Locate and identify every blood parasite.
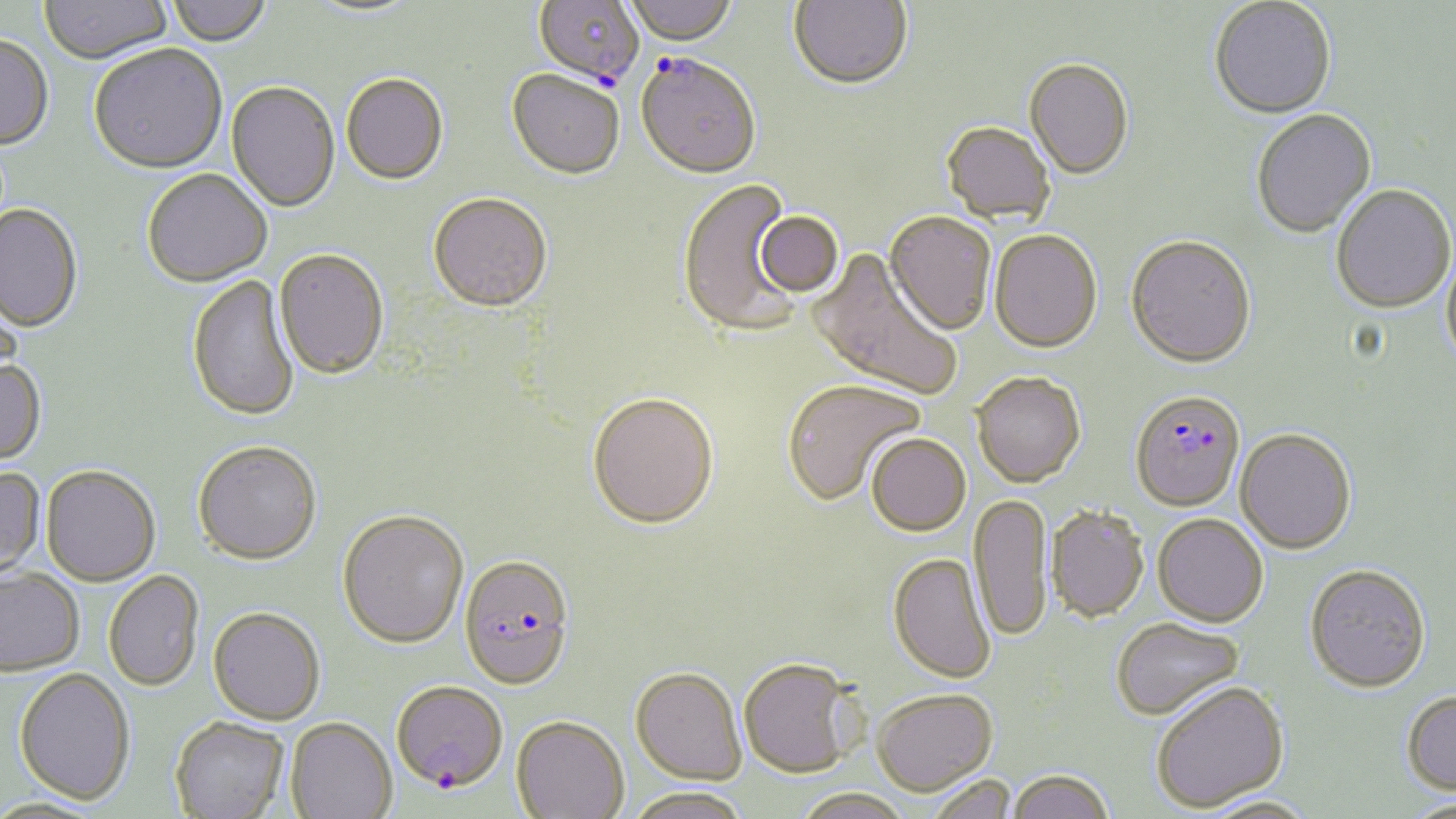
Approximate bounding boxes as (x1, y1, x2, y2) in pixels.
Plasmodium falciparum-infected red blood cells: (533, 0, 643, 91), (635, 57, 761, 182), (1130, 392, 1246, 514), (459, 556, 574, 693), (392, 682, 508, 794).
No Plasmodium ovale, Plasmodium malariae, Plasmodium vivax, Babesia divergens, or Trypanosoma brucei observed.

Uninfected red blood cell locations: (40, 0, 172, 67), (166, 0, 273, 49), (624, 0, 739, 49), (788, 0, 913, 93), (301, 1, 424, 21), (1209, 1, 1336, 121), (0, 36, 54, 152), (89, 48, 227, 176), (1024, 61, 1134, 182), (506, 72, 624, 182), (341, 76, 448, 187), (226, 84, 340, 214), (1252, 111, 1377, 240), (940, 123, 1055, 226), (142, 171, 272, 289), (677, 179, 805, 339), (1332, 186, 1455, 316), (428, 197, 553, 315), (0, 206, 83, 334), (755, 211, 844, 300), (884, 213, 996, 338), (990, 232, 1102, 356), (1125, 238, 1256, 371), (1442, 246, 1456, 375), (807, 248, 963, 402), (274, 251, 389, 381), (187, 275, 299, 423), (0, 358, 46, 468), (971, 375, 1085, 490), (782, 379, 925, 509), (587, 395, 719, 532), (1235, 430, 1357, 556), (865, 436, 971, 538), (192, 443, 322, 567), (41, 467, 161, 588), (0, 468, 46, 582), (969, 495, 1052, 644), (1045, 507, 1148, 625), (336, 512, 469, 650), (1152, 516, 1268, 629), (887, 555, 996, 686), (1305, 567, 1431, 695), (0, 568, 84, 677), (104, 571, 205, 692), (207, 609, 325, 726), (1111, 618, 1246, 723), (739, 660, 860, 781), (630, 667, 747, 785), (12, 670, 135, 808), (1151, 683, 1290, 813), (871, 690, 998, 798), (1401, 692, 1456, 796), (511, 717, 629, 819), (169, 718, 289, 818), (285, 719, 398, 819), (1007, 772, 1114, 819), (927, 774, 1019, 819), (625, 786, 752, 819), (791, 790, 914, 819), (1404, 795, 1456, 819), (1197, 797, 1321, 819). Slide-level diagnosis: Plasmodium falciparum. Single field of view. 1000x magnification. Thin blood film. Light microscopy. Image is 1456×819 pixels. May-Grünwald-Giemsa stain.